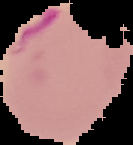

result = Plasmodium parasites identified
preparation = thin blood film
image type = segmented cell region on a black background
image size = 133×145 pixels